Give the extent of all Plasmodium falciparum-infected red blood cells.
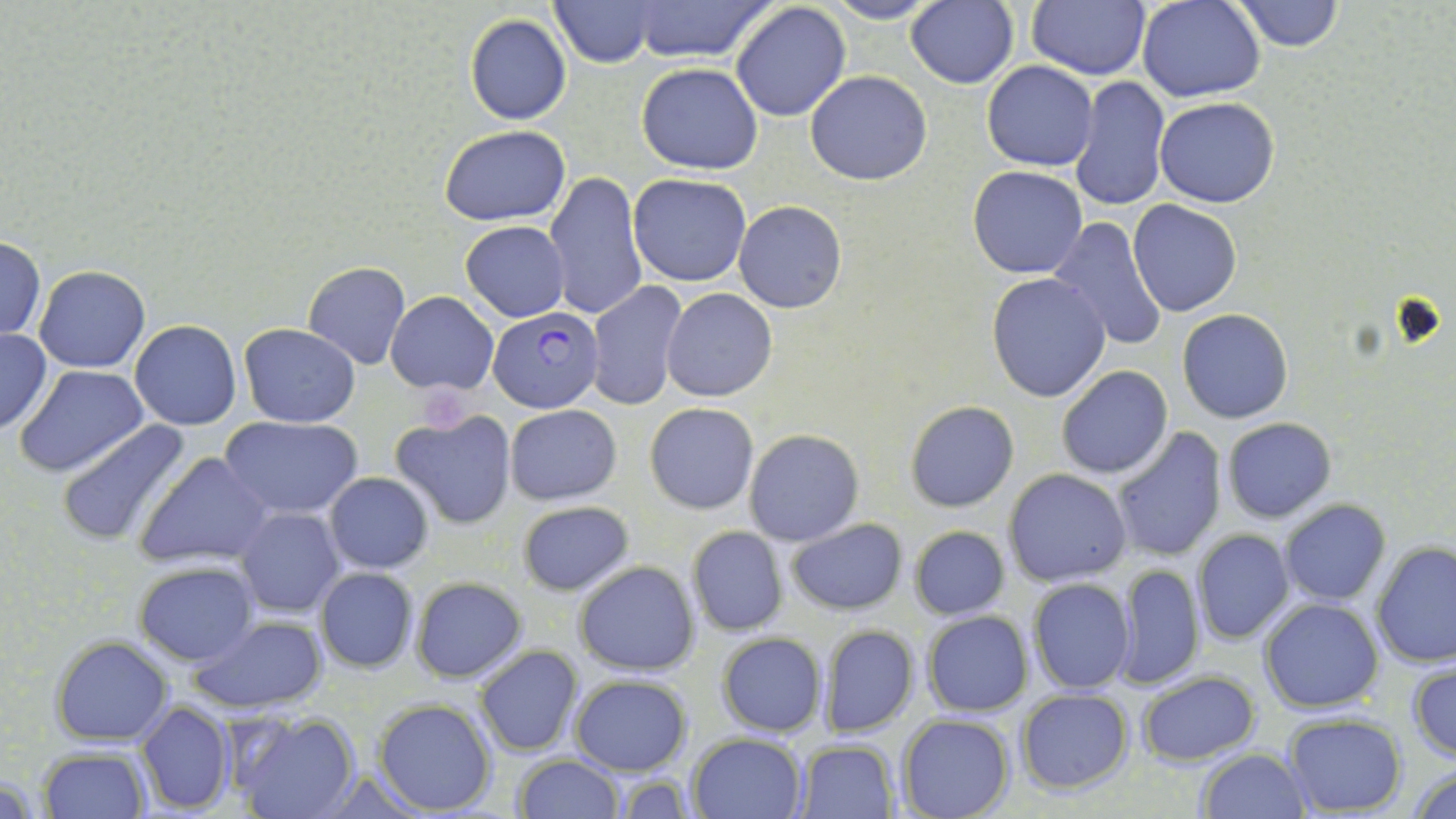
Approximate bounding boxes as (x1, y1, x2, y2) in pixels.
Plasmodium falciparum-infected red blood cells: (489, 308, 603, 413).

Summary:
  - Platelet locations: (422, 391, 467, 430)
  - Uninfected red blood cell locations: (548, 0, 660, 67), (631, 0, 773, 62), (823, 0, 942, 25), (1026, 0, 1148, 81), (1137, 0, 1266, 102), (1231, 0, 1345, 51), (905, 1, 1019, 88), (731, 2, 852, 121), (463, 15, 572, 124), (981, 61, 1099, 171), (637, 63, 763, 174), (805, 71, 932, 185), (1069, 75, 1171, 212), (1154, 97, 1280, 207), (439, 125, 571, 226), (968, 165, 1088, 278), (544, 171, 648, 322), (628, 172, 751, 286), (1128, 200, 1244, 317), (735, 201, 847, 314), (1047, 216, 1169, 353), (460, 221, 570, 321), (1, 236, 46, 340), (302, 261, 412, 369), (34, 265, 150, 373), (986, 272, 1113, 404), (586, 282, 692, 412), (661, 288, 777, 401), (386, 291, 499, 395), (1177, 310, 1293, 424), (130, 320, 241, 430), (239, 324, 361, 427), (0, 328, 50, 433), (15, 365, 150, 478), (1056, 365, 1174, 480), (905, 401, 1018, 512), (644, 402, 759, 515), (505, 404, 622, 505), (391, 409, 516, 530), (221, 415, 363, 519), (56, 418, 197, 547), (1221, 418, 1336, 524), (1109, 426, 1228, 562), (744, 428, 864, 546), (137, 454, 272, 567), (1004, 469, 1131, 587), (325, 472, 433, 572), (516, 500, 633, 595), (1279, 500, 1389, 604), (237, 508, 343, 617), (786, 517, 908, 615), (909, 524, 1010, 621), (687, 525, 789, 636), (1191, 528, 1295, 644), (1371, 540, 1456, 668), (574, 561, 700, 675), (135, 562, 257, 665), (1111, 563, 1206, 690), (315, 567, 417, 674), (409, 576, 526, 684), (1026, 578, 1135, 695), (1259, 597, 1385, 714), (922, 611, 1033, 716), (189, 615, 327, 712), (819, 624, 919, 738), (716, 632, 827, 739), (51, 636, 172, 746), (473, 645, 583, 756), (1408, 659, 1456, 763), (1137, 669, 1259, 766), (570, 673, 693, 775), (1016, 688, 1133, 792), (372, 698, 497, 816), (135, 701, 236, 815), (227, 709, 361, 819), (896, 713, 1015, 819), (1280, 714, 1406, 816), (687, 732, 807, 818), (798, 738, 899, 818), (1196, 747, 1309, 818), (38, 748, 149, 819), (513, 754, 623, 818), (1409, 765, 1456, 819)
  - Slide-level diagnosis: Plasmodium falciparum
  - Image size: 1456×819 pixels
  - Stain: May-Grünwald-Giemsa
  - Modality: optical microscopy
  - Preparation: thin blood film
  - Magnification: 1000x
  - Field of view: single